Assess this cell for malaria.
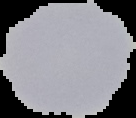
It is uninfected.

{
  "image_type": "segmented cell region with the area outside set to black",
  "image_size": "136×118 pixels",
  "preparation": "thin blood smear"
}